Outline each Plasmodium ovale-infected red blood cell.
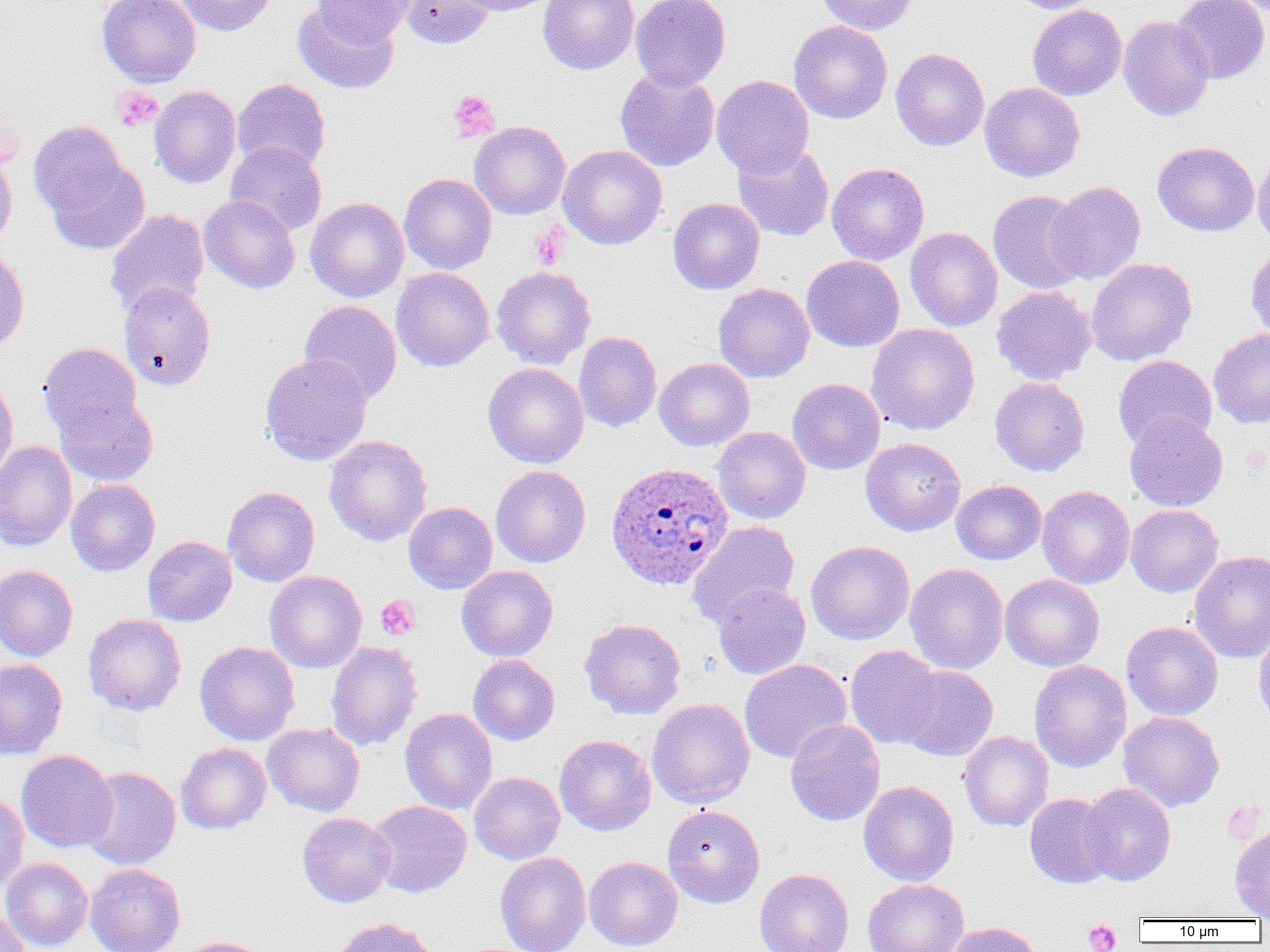

Approximate bounding boxes as (x1,y1)-(x2,y2) corner pairs in pixels.
Plasmodium ovale-infected red blood cells: (606,461)-(733,589).

Summary:
  - Platelet locations: (111,85)-(163,133), (448,90)-(500,142), (531,223)-(569,269), (375,595)-(420,640), (1082,920)-(1122,951)
  - Uninfected red blood cell locations: (98,0)-(201,88), (173,0)-(275,37), (312,0)-(415,45), (398,0)-(495,49), (451,0)-(561,16), (538,0)-(640,75), (630,0)-(731,91), (816,0)-(918,35), (1008,0)-(1103,14), (1171,0)-(1269,85), (293,3)-(399,94), (1027,4)-(1127,101), (1118,16)-(1215,121), (788,20)-(893,124), (890,48)-(989,151), (615,67)-(720,172), (711,74)-(814,177), (232,78)-(331,174), (979,82)-(1085,182), (149,85)-(241,188), (28,121)-(128,217), (469,121)-(571,220), (1152,141)-(1259,236), (225,142)-(327,236), (732,142)-(834,242), (558,145)-(667,250), (0,150)-(17,251), (1252,151)-(1270,252), (46,158)-(150,255), (826,162)-(929,265), (399,173)-(497,274), (1047,181)-(1146,284), (988,190)-(1091,293), (199,194)-(301,294), (306,197)-(409,302), (668,197)-(765,294), (105,209)-(209,316), (905,227)-(1002,331), (1246,246)-(1270,343), (0,248)-(29,353), (802,255)-(904,352), (1086,257)-(1197,366), (490,266)-(595,369), (391,267)-(495,372), (118,281)-(216,390), (713,283)-(814,383), (991,285)-(1097,385), (300,300)-(402,403), (866,323)-(980,435), (1208,328)-(1270,428), (574,331)-(662,433), (39,342)-(142,440), (260,353)-(373,466), (1113,355)-(1217,451), (654,358)-(755,451), (483,362)-(589,468), (989,376)-(1090,476), (0,377)-(18,484), (787,378)-(885,474), (54,393)-(159,487), (1124,413)-(1228,512), (713,426)-(810,523), (324,434)-(432,547), (860,437)-(966,536), (0,440)-(77,551), (491,465)-(591,568), (66,479)-(161,576), (951,480)-(1046,565), (1037,485)-(1135,589), (222,486)-(319,587), (404,502)-(498,594), (1125,504)-(1223,597), (687,520)-(800,628), (142,536)-(237,626), (805,540)-(915,645), (1189,550)-(1270,663), (904,563)-(1008,674), (0,564)-(78,662), (456,565)-(558,662), (264,570)-(367,673), (999,574)-(1105,672), (712,583)-(811,680), (83,613)-(187,716), (579,618)-(686,719), (1121,620)-(1223,721), (1253,625)-(1270,737), (194,640)-(300,745), (325,640)-(423,751), (844,645)-(943,749), (468,654)-(560,745), (0,658)-(67,759), (739,659)-(852,763), (1029,659)-(1131,772), (898,665)-(998,761), (647,698)-(755,808), (400,708)-(498,815), (1118,711)-(1224,811), (785,719)-(885,826), (263,723)-(365,816), (959,730)-(1054,832), (554,734)-(657,836), (175,742)-(271,834), (16,749)-(117,852), (82,766)-(181,870), (469,771)-(565,865), (858,780)-(959,886), (1081,782)-(1176,886), (0,790)-(29,894), (1025,793)-(1119,888), (367,800)-(472,898), (662,804)-(765,908), (297,812)-(396,907), (1229,823)-(1270,920), (495,852)-(591,952), (584,856)-(683,950), (1,857)-(93,951), (85,863)-(185,952), (754,868)-(854,952), (862,878)-(969,952), (0,905)-(31,952), (330,917)-(438,952), (943,921)-(1044,952), (179,936)-(271,952)
  - Slide-level diagnosis: Plasmodium ovale
  - Magnification: 1000x
  - Image size: 1270×952 pixels
  - Field of view: single
  - Preparation: thin blood film
  - Modality: optical microscopy